Describe the morphology of the erythrocytes.
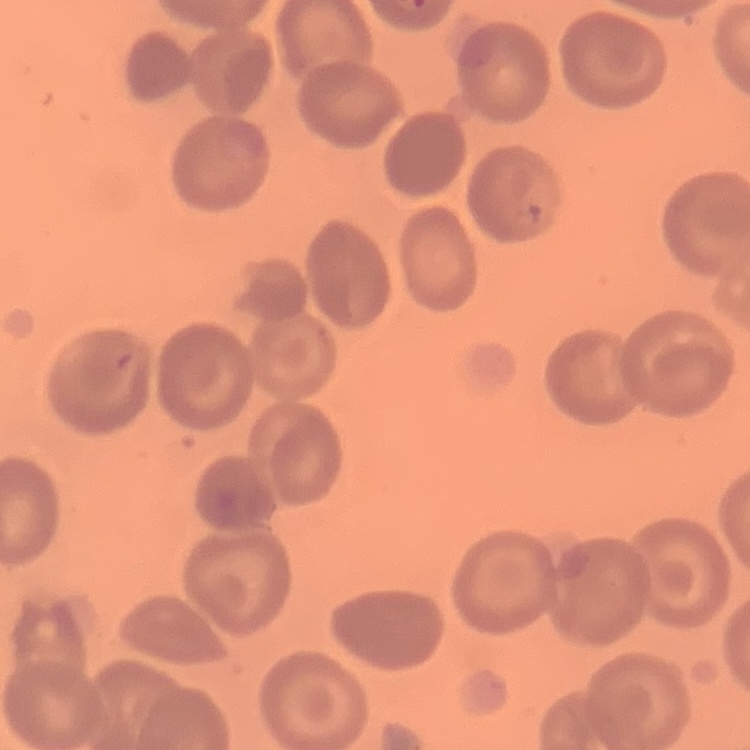
They show no rouleaux formation.

One tile cut from a larger photomicrograph. Thin blood film. Stained with either Field's or Giemsa.